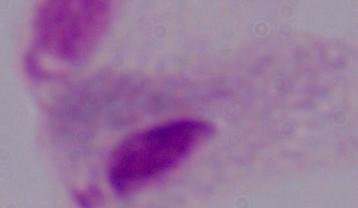

Micrograph. A trichomonad is shown. 1000x magnification.